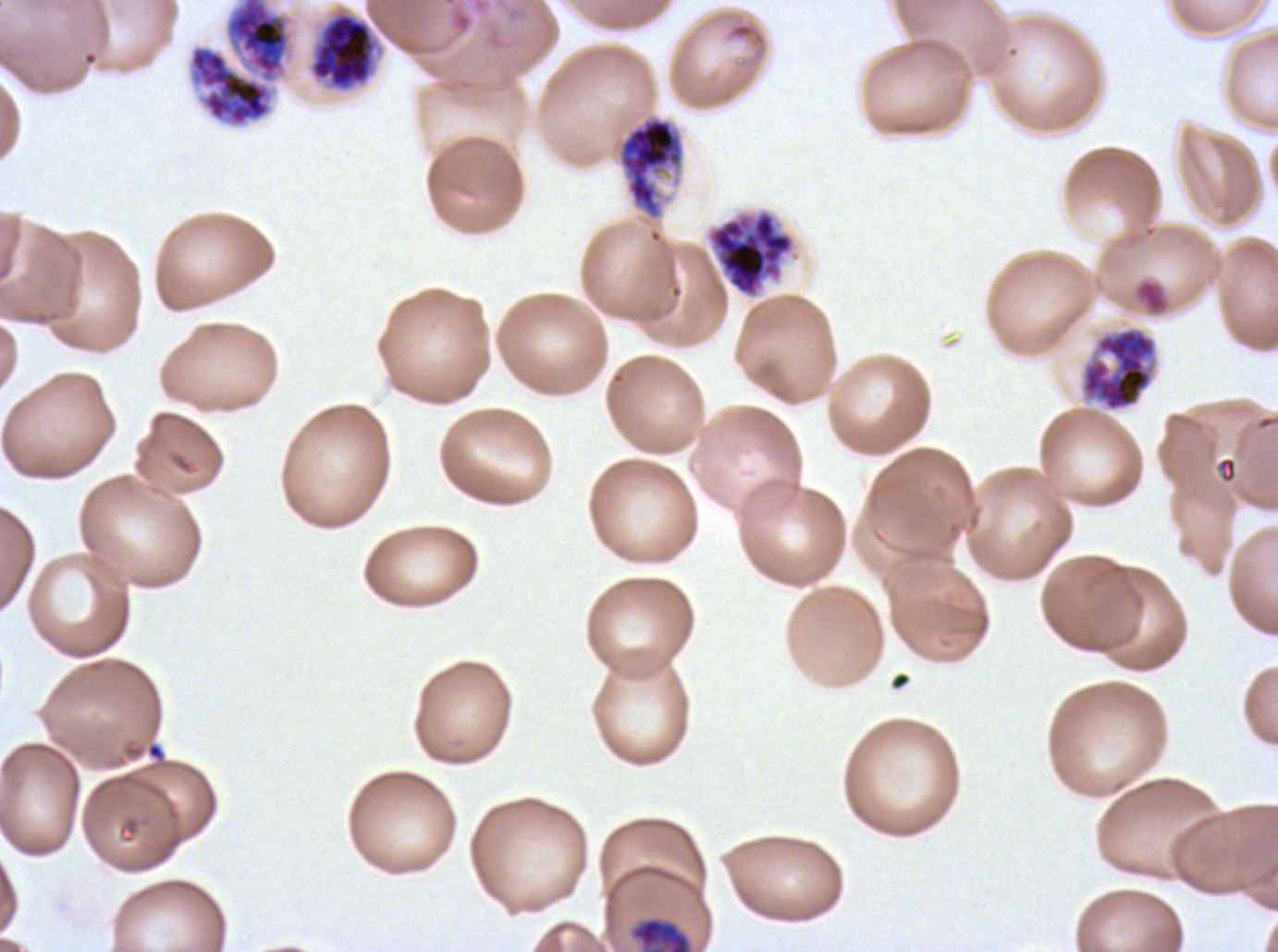

Approximate bounding rectangles given as corner coordinates in pixels from the top-left.
Summary:
  - Late schizont locations: (x1=188, y1=0, x2=293, y2=128), (x1=308, y1=9, x2=380, y2=92), (x1=1079, y1=325, x2=1158, y2=412)
  - Early schizont locations: (x1=614, y1=113, x2=686, y2=222), (x1=706, y1=208, x2=796, y2=299), (x1=630, y1=916, x2=693, y2=951)
  - Specimen: ex-vivo Plasmodium falciparum culture from a patient in The Gambia, grown for 24 to 48 hours
  - Image size: 1278×952 pixels
  - Preparation: thin blood smear
  - Life-cycle stages observed: early schizont, late schizont
  - Field of view: sub-image separated from a larger composite
  - Stain: Giemsa